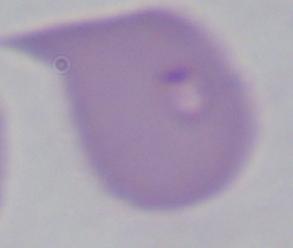
Summary:
  - Identification: Babesia
  - Magnification: 1000x
  - Modality: photomicrograph